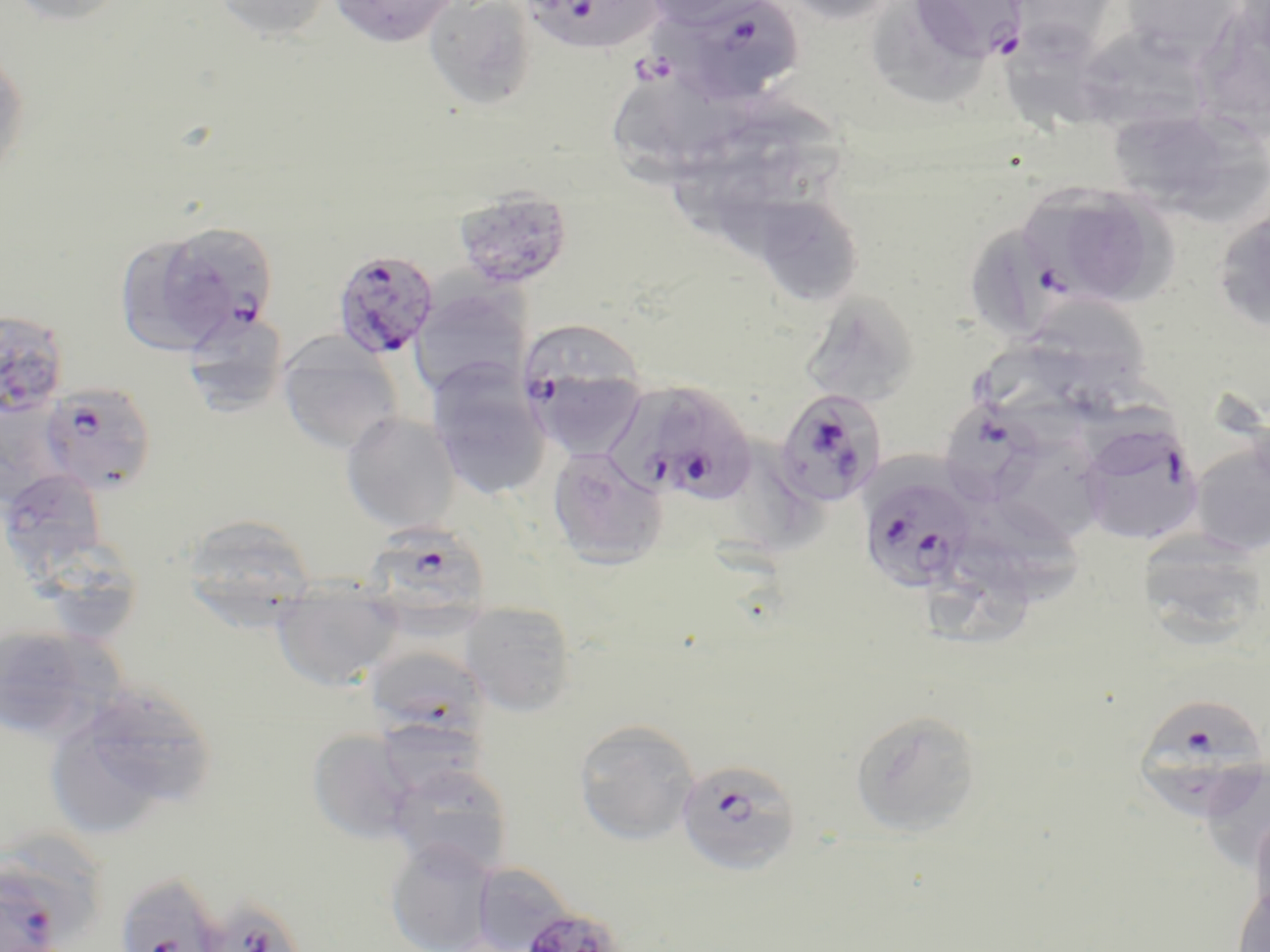 Approximate bounding boxes as (x1, y1, x2, y2) in pixels. Uninfected red blood cell locations: (5, 0, 132, 27), (211, 0, 334, 42), (328, 0, 460, 47), (423, 0, 539, 111), (641, 0, 771, 30), (778, 0, 902, 26), (871, 0, 995, 116), (1118, 0, 1247, 66), (1003, 1, 1125, 56), (1008, 21, 1129, 141), (1083, 23, 1199, 139), (0, 47, 29, 185), (612, 80, 735, 189), (1106, 108, 1259, 217), (679, 120, 803, 226), (452, 186, 573, 290), (1074, 189, 1184, 301), (766, 197, 863, 306), (1211, 203, 1270, 337), (969, 224, 1062, 347), (116, 237, 226, 361), (409, 283, 531, 399), (801, 292, 921, 407), (1040, 300, 1155, 410), (180, 309, 290, 415), (277, 334, 404, 455), (972, 334, 1089, 410), (425, 359, 552, 501), (0, 394, 73, 508), (340, 412, 460, 533), (1189, 439, 1270, 558), (996, 441, 1105, 539), (547, 447, 669, 569), (0, 468, 107, 569), (962, 496, 1082, 606), (180, 513, 317, 625), (1135, 533, 1268, 649), (40, 537, 142, 642), (926, 538, 1037, 650), (271, 586, 403, 691), (459, 601, 578, 716), (0, 624, 126, 744), (363, 645, 492, 748), (58, 681, 218, 824), (849, 708, 983, 838), (376, 717, 488, 799), (572, 719, 701, 846), (306, 728, 422, 845), (387, 762, 513, 876), (1208, 763, 1270, 862), (1249, 805, 1270, 926), (0, 836, 107, 952), (385, 839, 499, 952), (469, 864, 577, 950), (1231, 883, 1270, 952). Plasmodium falciparum-infected red blood cell locations: (520, 0, 661, 55), (907, 0, 1028, 64), (665, 1, 805, 105), (1018, 185, 1141, 306), (171, 227, 276, 344), (331, 249, 440, 360), (0, 309, 69, 417), (518, 321, 651, 456), (39, 380, 158, 495), (606, 381, 713, 502), (661, 387, 760, 506), (773, 388, 886, 509), (944, 400, 1043, 512), (1078, 421, 1205, 546), (859, 471, 975, 594), (361, 519, 495, 628), (1130, 692, 1270, 822), (675, 757, 801, 877), (0, 868, 66, 952), (113, 871, 235, 952), (205, 904, 302, 952), (518, 906, 627, 952). Slide-level diagnosis: Plasmodium falciparum. Captured at 1000x magnification. May-Grünwald-Giemsa stain. Image is 1270×952 pixels. Optical microscopy. Single field of view. Thin blood smear.